Identify the parasite.
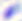

Toxoplasma gondii.

magnification = 400x
modality = micrograph